Assess the morphology of the erythrocytes.
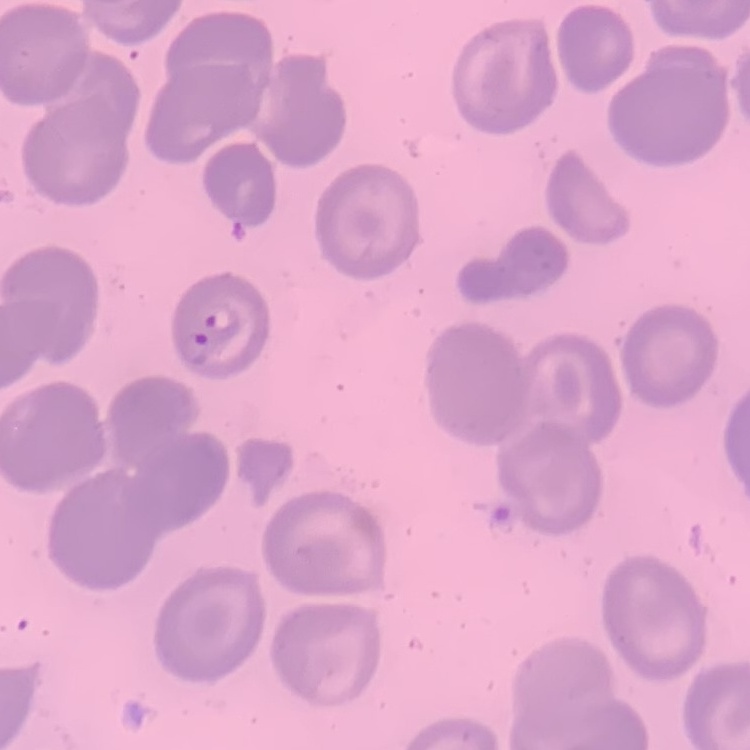
They show no rouleaux formation.

Thin blood smear. One tile cut from a larger photomicrograph. Field's or Giemsa stain.